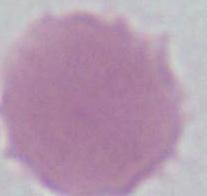

Summary:
  - Modality: photomicrograph
  - Magnification: 1000x
  - Identification: red blood cell